Assess this cell for malaria.
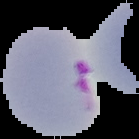

Parasitized.

{
  "preparation": "thin blood film",
  "image_type": "segmented cell region with the area outside set to black",
  "image_size": "139×139 pixels"
}